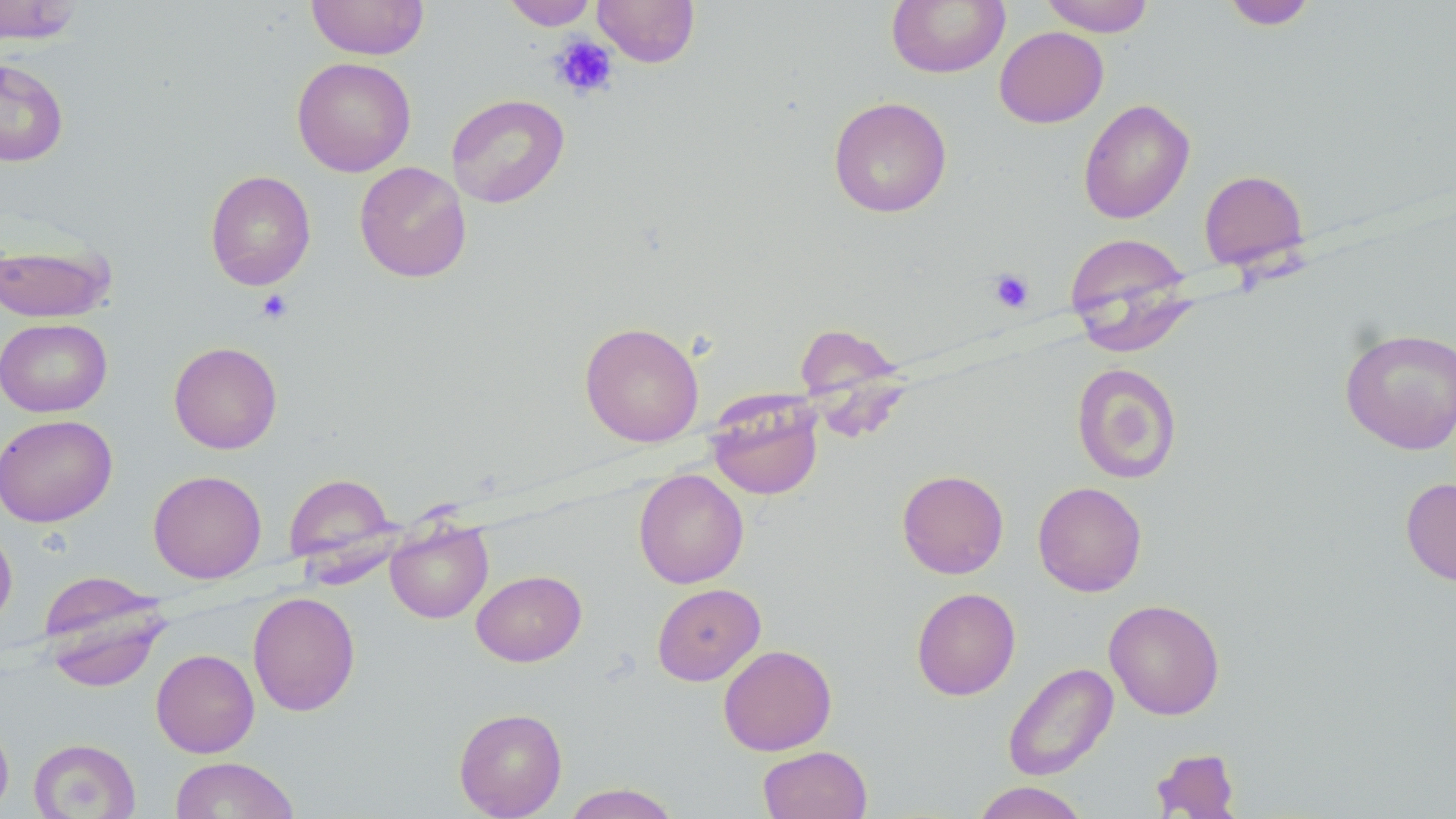

Summary:
  - Coordinate format: approximate bounding boxes as (x1, y1, x2, y2) in pixels
  - Platelet locations: (549, 34, 619, 100), (989, 269, 1035, 313), (257, 289, 293, 323)
  - Uninfected red blood cell locations: (0, 0, 83, 45), (306, 0, 429, 60), (501, 0, 598, 30), (592, 0, 700, 67), (887, 0, 1010, 78), (1039, 0, 1155, 37), (1221, 0, 1317, 30), (994, 26, 1108, 128), (291, 57, 416, 177), (0, 59, 69, 167), (446, 93, 569, 208), (828, 96, 952, 218), (1078, 98, 1195, 225), (355, 161, 471, 283), (1198, 169, 1309, 271), (205, 170, 316, 290), (1064, 232, 1196, 349), (0, 240, 115, 323), (0, 318, 112, 417), (580, 321, 704, 446), (792, 323, 907, 420), (1339, 327, 1456, 455), (169, 341, 283, 454), (1071, 363, 1183, 484), (706, 395, 823, 500), (0, 414, 117, 526), (633, 469, 749, 588), (896, 469, 1009, 579), (148, 470, 267, 583), (283, 473, 397, 569), (1400, 477, 1456, 586), (1033, 481, 1147, 597), (385, 518, 493, 623), (0, 525, 17, 630), (471, 570, 587, 667), (40, 579, 169, 692), (651, 583, 766, 686), (911, 587, 1021, 701), (247, 591, 360, 716), (1104, 599, 1225, 720), (718, 644, 837, 756), (151, 649, 259, 758), (1003, 662, 1119, 781), (454, 707, 567, 819), (0, 715, 14, 817), (28, 738, 141, 819), (758, 745, 872, 819), (1151, 747, 1241, 818), (169, 757, 300, 819), (970, 781, 1091, 819), (562, 783, 681, 819)
  - Slide-level diagnosis: no evidence of blood parasites
  - Magnification: 1000x
  - Image size: 1456×819 pixels
  - Field of view: one of a larger specimen
  - Stain: May-Grünwald-Giemsa
  - Preparation: thin blood smear
  - Modality: light microscopy